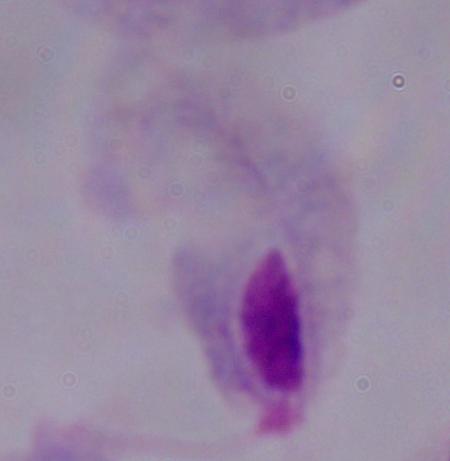
Summary:
  - Modality: photomicrograph
  - Identification: trichomonad
  - Magnification: 1000x